Describe the morphology of the red blood cells.
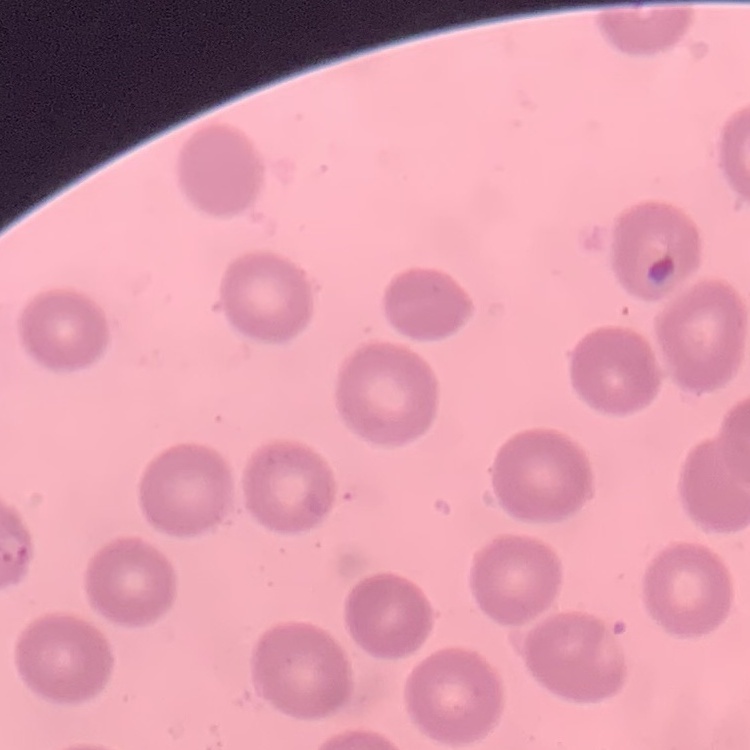
They show no rouleaux formation.

Summary:
  - Stain: Field's or Giemsa
  - Image type: one tile cut from a larger photomicrograph
  - Preparation: thin blood smear